Assess the morphology of the red blood cells.
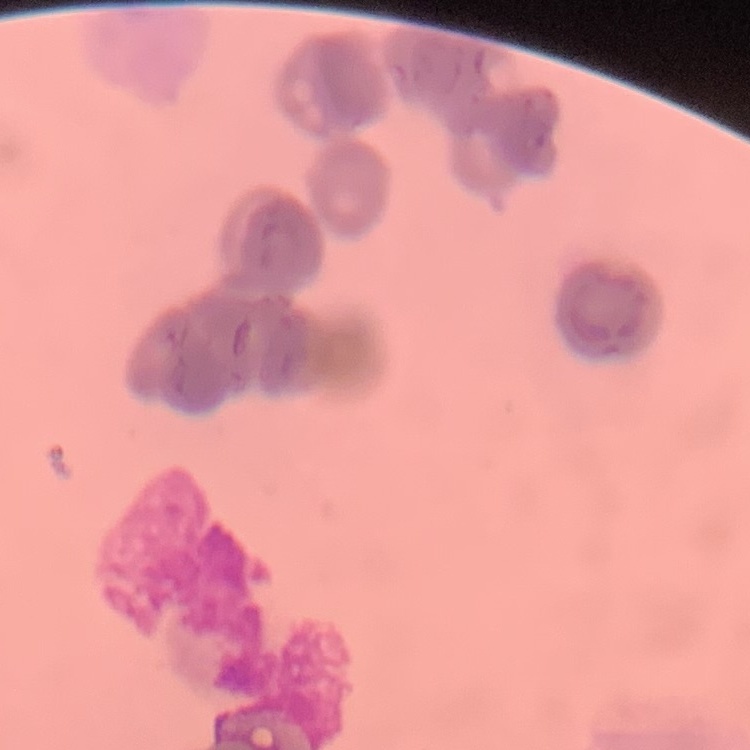

Rouleaux formation.

Summary:
  - Preparation: thin blood smear
  - Stain: Field's or Giemsa
  - Image type: square crop of a larger photomicrograph